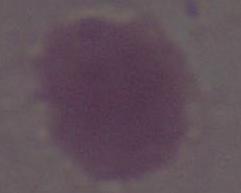 Micrograph. An erythrocyte is shown. Captured at 1000x magnification.